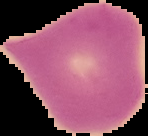

Summary:
  - Preparation: thin blood smear
  - Malaria status: uninfected
  - Image type: segmented cell region with the area outside set to black
  - Image size: 148×136 pixels